Give the preparation type.
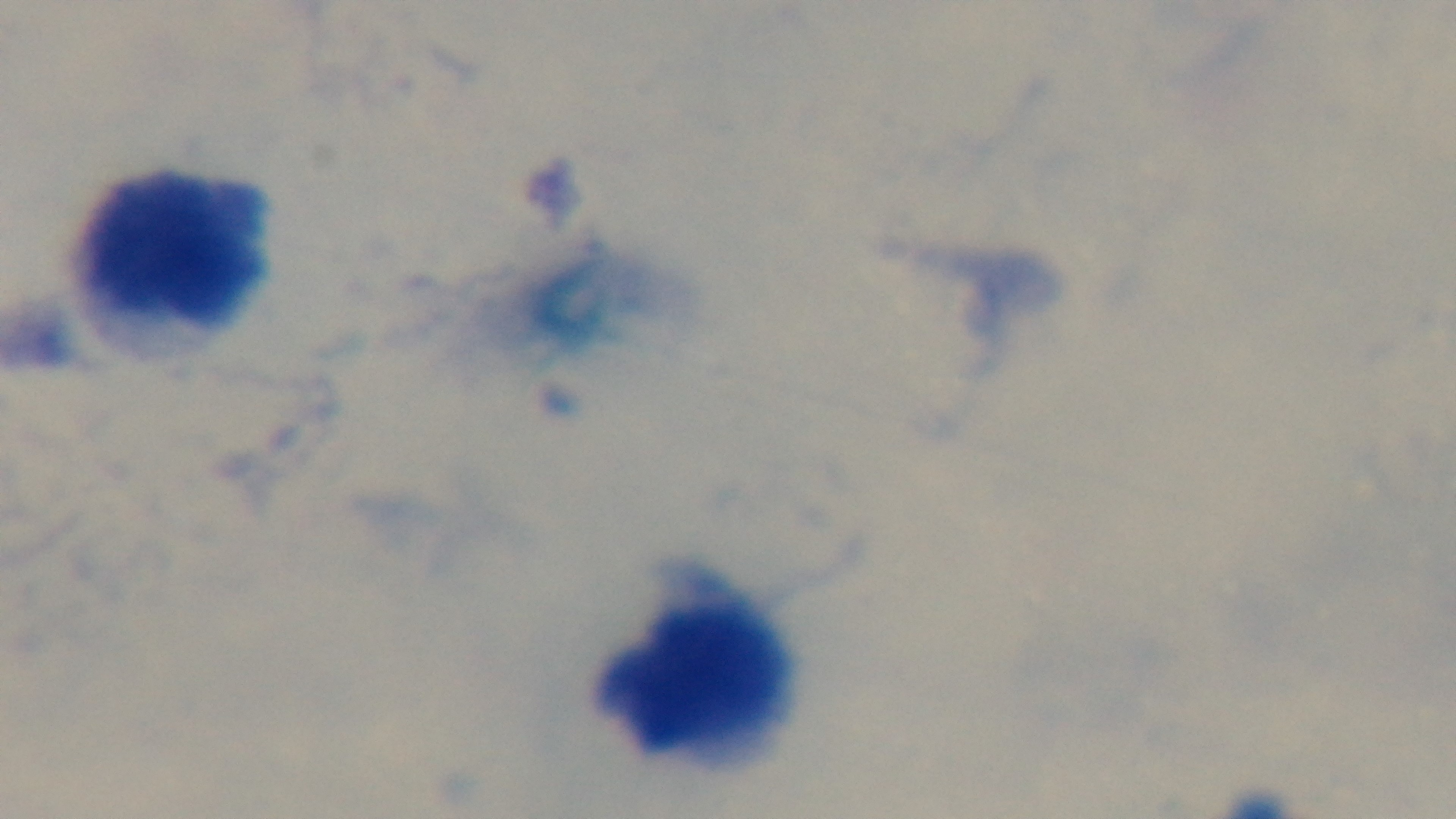

Thick.

Summary:
  - Malaria status: uninfected
  - Field of view: single
  - Capture: mounted 4K digital camera
  - Modality: light microscopy
  - Stain: Giemsa
  - Objective: 100x oil immersion